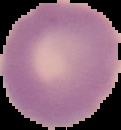
{
  "preparation": "thin blood smear",
  "image_size": "121×130 pixels",
  "malaria_status": "uninfected",
  "image_type": "segmented cell region on a black background"
}